Locate every blood parasite and identify its species.
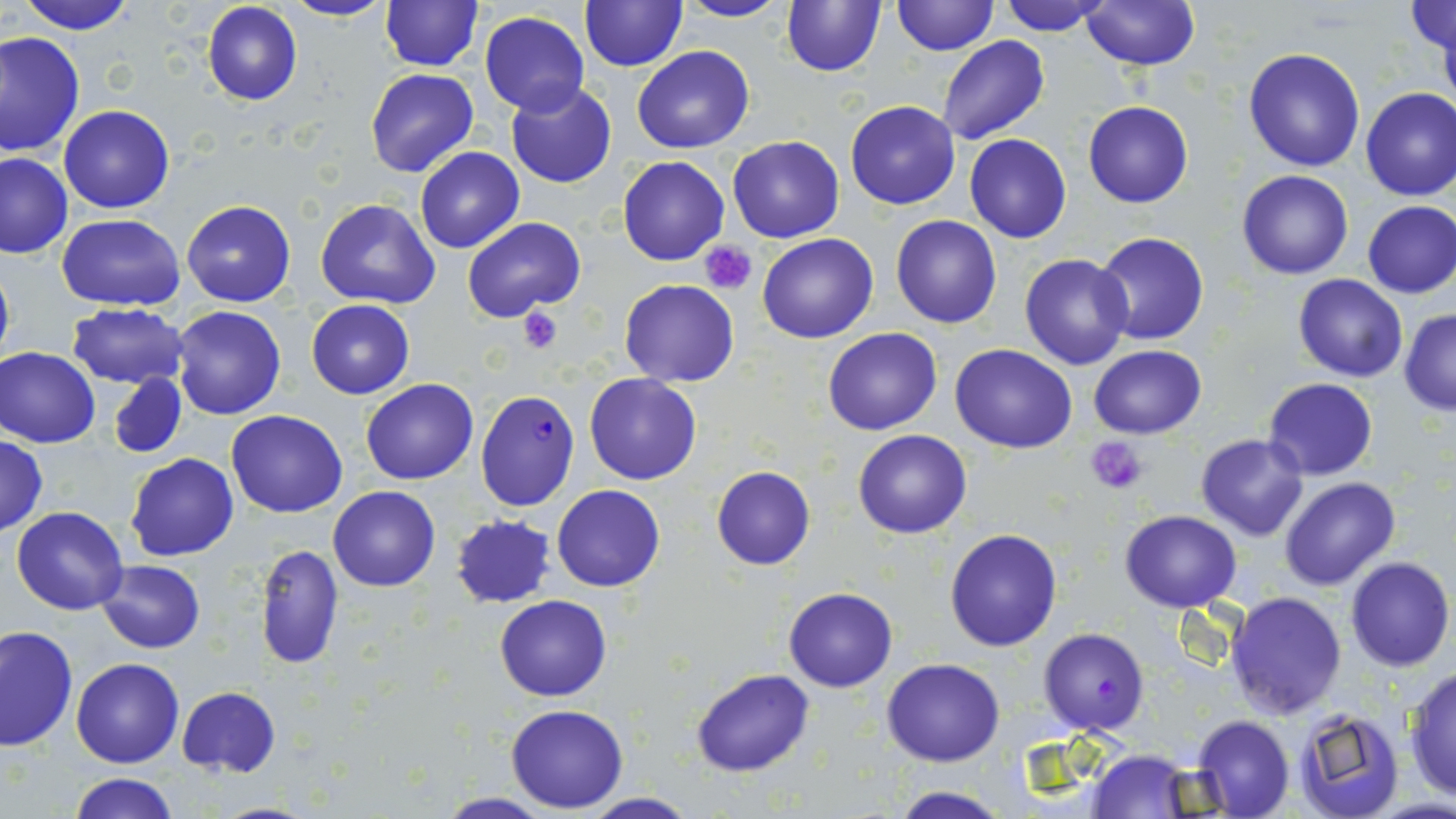

Approximate bounding boxes as [x1, y1, x2, y2] in pixels.
Plasmodium falciparum-infected red blood cells: [473, 391, 580, 510], [1038, 627, 1149, 734].
No Plasmodium ovale, Plasmodium malariae, Plasmodium vivax, Babesia divergens, or Trypanosoma brucei observed.

slide-level diagnosis = Plasmodium falciparum
modality = light microscopy
preparation = thin blood smear
magnification = 1000x
uninfected red blood cell locations = approximate bounding boxes as [x1, y1, x2, y2] in pixels: [16, 0, 136, 35], [283, 0, 395, 23], [673, 0, 793, 23], [780, 0, 885, 77], [201, 1, 302, 105], [380, 1, 482, 70], [892, 1, 997, 56], [995, 1, 1110, 35], [1079, 1, 1201, 71], [580, 2, 687, 71], [1405, 3, 1456, 55], [479, 11, 589, 115], [1436, 14, 1455, 111], [0, 32, 82, 154], [937, 35, 1050, 146], [632, 45, 755, 153], [1243, 47, 1366, 172], [365, 68, 478, 176], [506, 81, 617, 189], [1359, 86, 1456, 200], [846, 100, 961, 210], [1083, 101, 1193, 208], [59, 105, 175, 214], [964, 134, 1072, 242], [726, 136, 844, 243], [415, 147, 523, 253], [0, 153, 74, 259], [618, 155, 730, 266], [1236, 170, 1354, 280], [315, 199, 440, 309], [1361, 200, 1456, 299], [181, 201, 296, 307], [57, 213, 185, 309], [892, 214, 1001, 328], [462, 216, 585, 321], [757, 233, 879, 343], [1091, 233, 1211, 345], [1019, 253, 1134, 370], [0, 257, 15, 377], [1293, 274, 1408, 382], [620, 279, 739, 386], [306, 299, 414, 399], [66, 302, 192, 388], [171, 304, 286, 420], [1400, 309, 1456, 415], [822, 327, 942, 436], [950, 344, 1078, 452], [1088, 345, 1206, 439], [0, 346, 100, 448], [108, 372, 189, 459], [584, 373, 702, 485], [1263, 377, 1378, 479], [360, 378, 480, 485], [226, 410, 348, 518], [853, 428, 972, 539], [1196, 433, 1308, 540], [0, 438, 47, 536], [126, 453, 238, 561], [711, 467, 816, 569], [1280, 475, 1400, 590], [552, 484, 665, 592], [329, 485, 439, 592], [11, 505, 128, 615], [1120, 509, 1241, 611], [450, 515, 557, 607], [944, 529, 1062, 651], [255, 543, 344, 671], [1344, 557, 1454, 671], [97, 559, 205, 652], [783, 588, 897, 692], [1226, 591, 1348, 718], [495, 594, 611, 701], [1, 624, 77, 751], [71, 657, 185, 768], [882, 659, 1004, 766], [1403, 665, 1456, 803], [693, 668, 814, 777], [176, 686, 282, 777], [505, 703, 628, 812], [1292, 709, 1406, 819], [1191, 716, 1294, 819], [1088, 747, 1195, 817], [69, 774, 177, 819], [886, 786, 1016, 819], [576, 792, 701, 818], [432, 793, 560, 819]
field of view = one of a larger specimen
stain = May-Grünwald-Giemsa
platelet locations = approximate bounding boxes as [x1, y1, x2, y2] in pixels: [700, 240, 756, 293], [516, 305, 561, 353], [1085, 437, 1147, 493]
image size = 1456×819 pixels